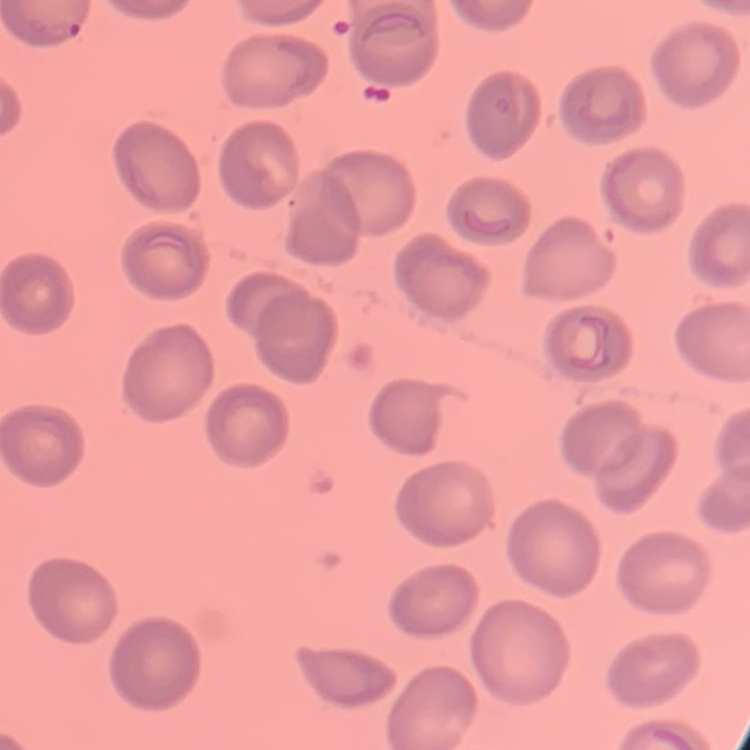
erythrocyte morphology = no rouleaux formation
stain = Field's or Giemsa
image type = one tile cut from a larger photomicrograph
preparation = thin blood film